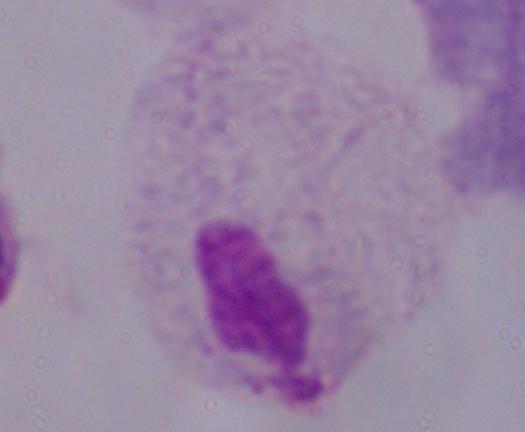
Photomicrograph. A trichomonad is shown. 1000x magnification.